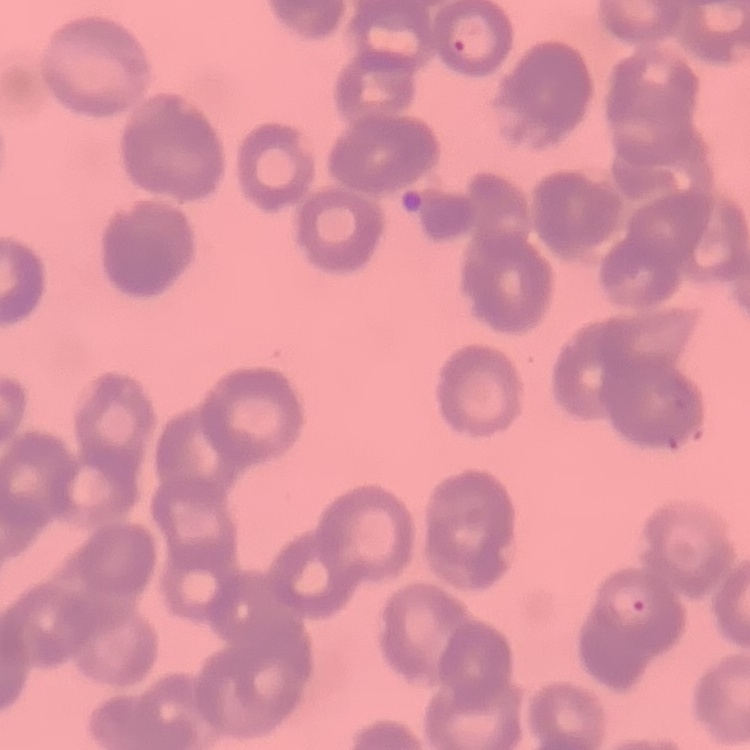

Summary:
  - Red blood cell morphology: rouleaux formation
  - Preparation: thin peripheral smear
  - Image type: square crop of a larger photomicrograph
  - Stain: Field's or Giemsa